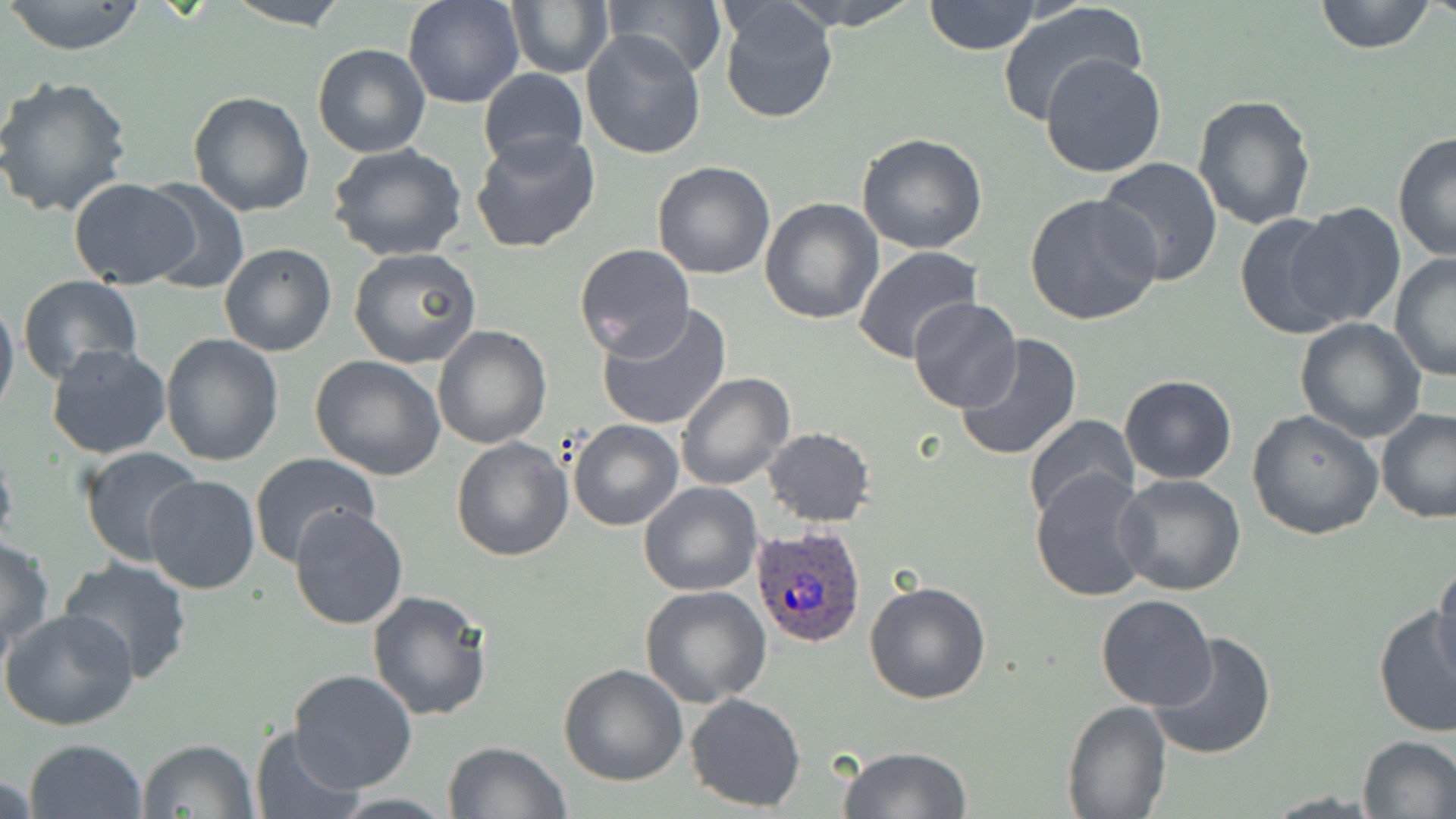
Summary:
  - Coordinate format: approximate bounding boxes as (x1, y1, x2, y2) in pixels
  - Uninfected red blood cell locations: (4, 0, 151, 56), (223, 0, 353, 29), (402, 0, 525, 109), (505, 0, 612, 79), (601, 0, 727, 80), (779, 0, 921, 29), (1314, 0, 1438, 54), (923, 1, 1041, 55), (997, 1, 1148, 124), (716, 3, 840, 124), (581, 32, 707, 159), (312, 44, 431, 159), (1039, 52, 1167, 177), (477, 67, 588, 169), (0, 76, 134, 218), (187, 90, 314, 217), (1191, 93, 1316, 232), (472, 130, 602, 256), (1394, 131, 1455, 264), (856, 133, 988, 255), (328, 145, 469, 262), (1095, 157, 1223, 288), (652, 160, 777, 279), (68, 178, 200, 287), (135, 178, 251, 295), (1023, 193, 1165, 328), (759, 198, 884, 325), (1288, 203, 1404, 329), (1234, 210, 1354, 340), (219, 243, 337, 357), (575, 243, 695, 358), (851, 246, 985, 366), (349, 247, 481, 368), (1390, 251, 1456, 381), (17, 274, 140, 381), (0, 295, 19, 418), (908, 296, 1022, 414), (596, 304, 732, 432), (1295, 318, 1427, 441), (432, 324, 554, 448), (160, 333, 285, 466), (954, 335, 1083, 462), (46, 343, 172, 460), (308, 355, 446, 480), (676, 373, 795, 491), (1118, 374, 1237, 484), (1377, 407, 1456, 524), (1248, 409, 1383, 540), (1025, 415, 1141, 522), (567, 420, 684, 532), (761, 427, 878, 526), (450, 436, 573, 561), (0, 444, 18, 557), (77, 446, 205, 569), (251, 454, 381, 568), (1032, 470, 1153, 601), (1115, 472, 1247, 595), (144, 474, 260, 594), (639, 483, 762, 597), (287, 505, 411, 631), (1, 538, 54, 654), (59, 556, 194, 683), (1428, 568, 1456, 684), (864, 578, 993, 704), (640, 586, 771, 706), (367, 590, 495, 722), (1096, 594, 1218, 711), (1373, 603, 1454, 740), (1, 607, 140, 733), (1148, 629, 1277, 759), (558, 663, 687, 786), (289, 668, 418, 792), (684, 691, 808, 812), (1062, 700, 1172, 818), (249, 726, 365, 816), (1357, 735, 1456, 818), (23, 738, 147, 819), (137, 738, 258, 819), (442, 741, 569, 818), (838, 746, 973, 818)
  - Plasmodium ovale-infected red blood cell locations: (749, 526, 867, 650)
  - Slide-level diagnosis: Plasmodium ovale
  - Image size: 1456×819 pixels
  - Modality: light microscopy
  - Magnification: 1000x
  - Field of view: one of a larger specimen
  - Preparation: thin blood film
  - Stain: May-Grünwald-Giemsa